Assess this cell for malaria.
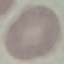
It is uninfected.

Summary:
  - Preparation: thin blood smear
  - Image type: automatically extracted cell patch, resized to 64 × 64 pixels
  - Stain: Giemsa
  - Capture: smartphone camera at the microscope eyepiece